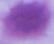 Micrograph. An erythrocyte is shown. 1000x magnification.